Outline each blood parasite and name the species.
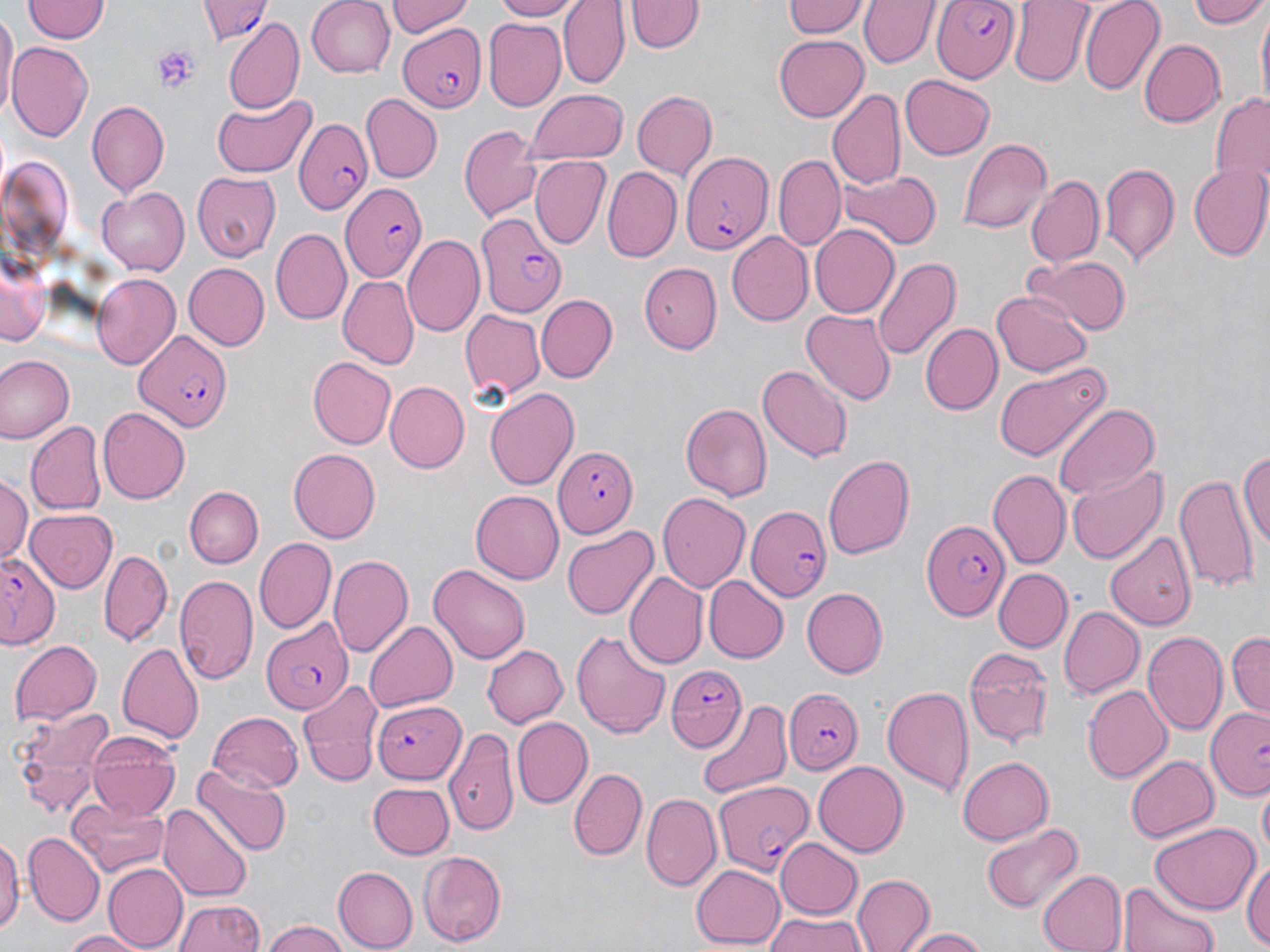

Approximate bounding boxes as (x1, y1, x2, y2) in pixels.
Plasmodium falciparum-infected red blood cells: (200, 0, 268, 45), (930, 0, 1021, 79), (397, 23, 485, 111), (295, 116, 371, 214), (679, 151, 770, 254), (341, 183, 428, 283), (476, 210, 566, 316), (134, 328, 231, 431), (551, 443, 638, 537), (748, 505, 832, 600), (922, 519, 1009, 622), (0, 550, 61, 648), (262, 621, 353, 712), (664, 664, 747, 754), (782, 686, 862, 776), (373, 699, 464, 783), (1205, 708, 1270, 803), (715, 783, 816, 875).
No Plasmodium ovale, Plasmodium malariae, Plasmodium vivax, Babesia divergens, or Trypanosoma brucei observed.

Summary:
  - Uninfected red blood cell locations: (23, 0, 108, 43), (307, 0, 396, 77), (387, 0, 476, 37), (486, 0, 583, 21), (558, 0, 629, 87), (780, 0, 868, 39), (861, 0, 937, 68), (1008, 0, 1096, 87), (1080, 0, 1164, 95), (1189, 0, 1270, 29), (627, 1, 702, 55), (1254, 8, 1269, 109), (1, 13, 17, 122), (223, 18, 305, 111), (483, 19, 566, 108), (773, 32, 868, 120), (1140, 39, 1226, 127), (9, 42, 92, 142), (899, 75, 994, 159), (827, 88, 906, 192), (524, 89, 629, 163), (631, 90, 718, 182), (1207, 92, 1270, 199), (362, 94, 442, 183), (210, 96, 314, 176), (87, 99, 170, 196), (458, 123, 544, 224), (959, 136, 1051, 234), (774, 154, 848, 249), (530, 157, 609, 249), (1100, 161, 1179, 268), (1187, 164, 1270, 261), (602, 168, 681, 264), (839, 170, 943, 252), (192, 171, 280, 259), (1026, 174, 1105, 269), (98, 186, 188, 275), (811, 226, 899, 317), (270, 227, 351, 325), (725, 232, 813, 327), (402, 236, 484, 335), (1, 253, 50, 348), (870, 255, 962, 362), (1024, 257, 1130, 336), (640, 261, 720, 354), (183, 263, 269, 350), (90, 274, 179, 368), (338, 276, 418, 369), (991, 292, 1090, 377), (536, 295, 617, 382), (459, 310, 545, 405), (803, 310, 895, 406), (919, 323, 1001, 414), (0, 355, 75, 444), (308, 359, 395, 450), (993, 360, 1111, 463), (757, 366, 852, 463), (384, 381, 468, 472), (485, 387, 578, 492), (679, 401, 773, 502), (1054, 403, 1160, 500), (98, 407, 189, 503), (28, 424, 106, 514), (288, 448, 381, 542), (1239, 448, 1270, 554), (823, 454, 915, 559), (1068, 464, 1165, 564), (988, 469, 1069, 570), (1174, 472, 1260, 596), (0, 477, 32, 565), (186, 487, 263, 569), (469, 490, 563, 585), (657, 493, 750, 590), (24, 509, 118, 593), (561, 525, 659, 617), (1105, 530, 1196, 631), (254, 537, 336, 633), (100, 550, 172, 646), (329, 553, 413, 655), (428, 563, 533, 665), (995, 568, 1070, 652), (626, 571, 706, 667), (174, 576, 258, 688), (704, 578, 787, 662), (802, 588, 888, 678), (1057, 605, 1144, 697), (362, 619, 457, 713), (571, 628, 672, 739), (1141, 628, 1227, 736), (1228, 631, 1269, 717), (9, 636, 102, 724), (118, 643, 203, 744), (481, 645, 569, 728), (963, 646, 1053, 747), (296, 680, 384, 787), (881, 682, 975, 798), (1083, 685, 1172, 783), (695, 700, 794, 802), (8, 703, 117, 816), (209, 710, 305, 791), (512, 717, 592, 807), (444, 721, 520, 839), (87, 733, 182, 822), (1126, 754, 1217, 844), (958, 757, 1054, 843), (813, 760, 909, 856), (192, 762, 291, 855), (570, 767, 646, 860), (366, 781, 456, 859), (1257, 786, 1269, 860), (641, 794, 720, 890), (65, 801, 170, 876), (158, 804, 252, 900), (980, 821, 1085, 913), (1151, 824, 1260, 913), (0, 832, 20, 939), (24, 833, 102, 925), (775, 837, 863, 917), (421, 850, 506, 945), (1243, 853, 1270, 952), (103, 864, 187, 949), (692, 864, 784, 947), (333, 867, 417, 950), (1036, 868, 1126, 952), (852, 873, 933, 952), (1117, 880, 1222, 952), (173, 898, 263, 952), (757, 913, 872, 952), (262, 923, 352, 952), (899, 926, 993, 951), (59, 928, 153, 951)
  - Platelet locations: (152, 45, 200, 92)
  - Slide-level diagnosis: Plasmodium falciparum
  - Field of view: one of a larger specimen
  - Image size: 1270×952 pixels
  - Preparation: thin blood film
  - Modality: light microscopy
  - Stain: May-Grünwald-Giemsa
  - Magnification: 1000x